State which cell type is depicted.
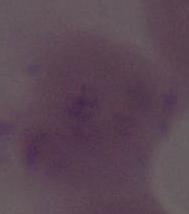
An erythrocyte.

Summary:
  - Magnification: 1000x
  - Modality: micrograph